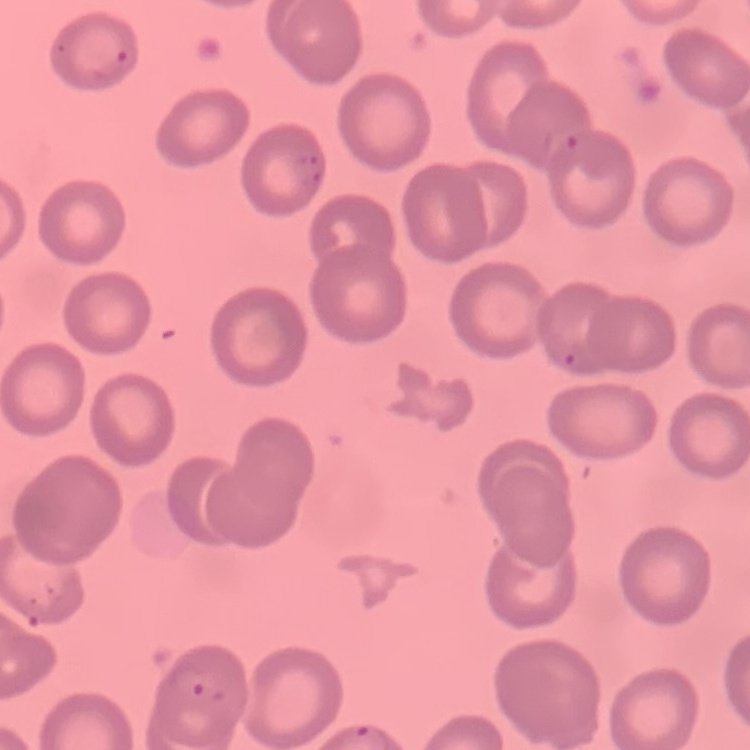
Summary:
  - Red blood cell morphology: no rouleaux formation
  - Preparation: thin peripheral smear
  - Stain: Field's or Giemsa
  - Image type: one tile cut from a larger photomicrograph